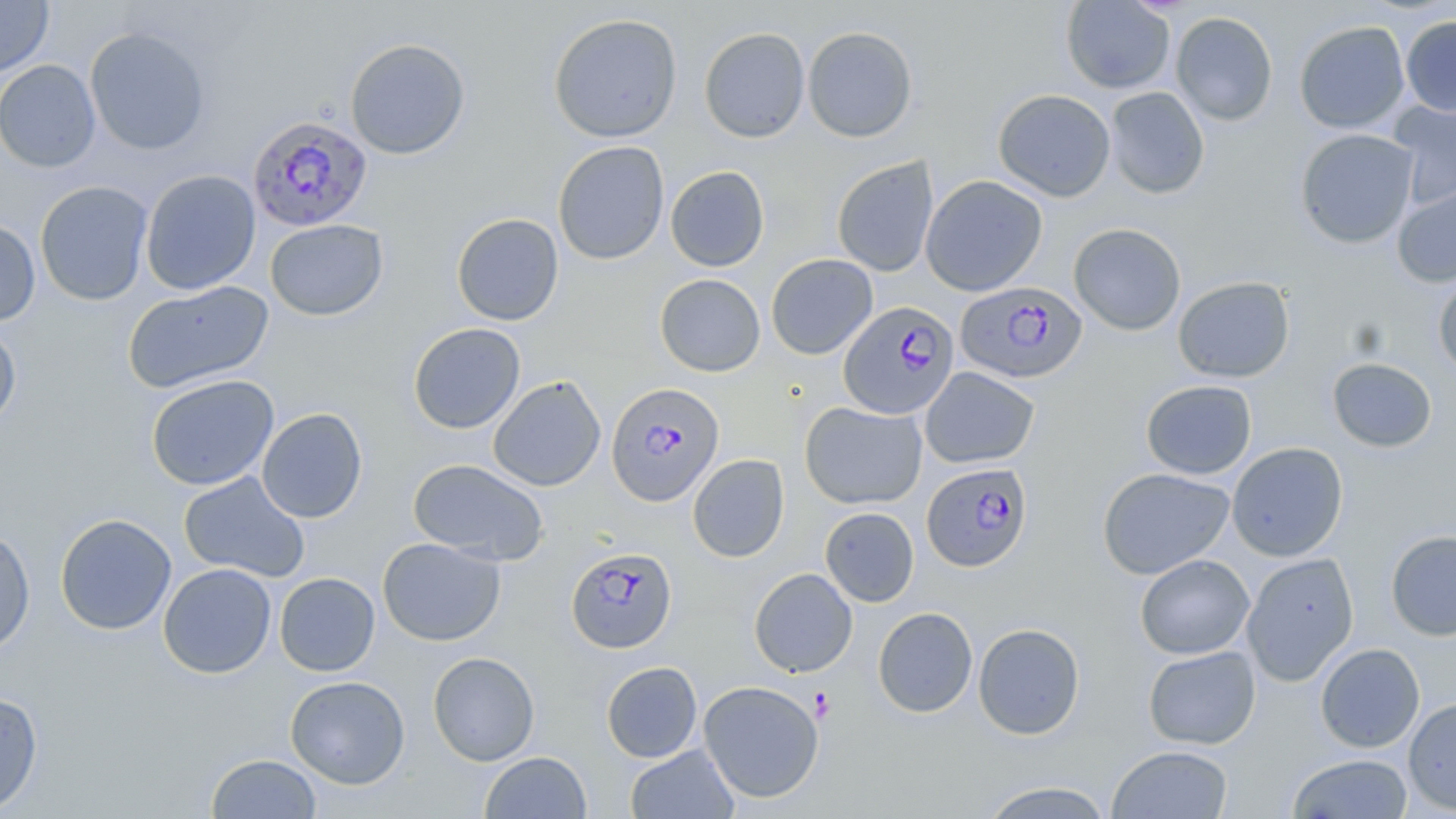
slide_level_diagnosis: Plasmodium falciparum
field_of_view: one of a larger specimen
magnification: 1000x
uninfected_red_blood_cell_locations: 'approximate bounding boxes as (x1,y1)-(x2,y2) corner pairs in pixels: (0,0)-(54,77), (1061,0)-(1176,94), (1170,11)-(1278,126), (548,12)-(683,143), (1400,15)-(1456,117), (1294,20)-(1410,134), (803,26)-(917,142), (84,27)-(210,155), (699,27)-(810,142), (345,37)-(471,160), (0,59)-(101,173), (1104,86)-(1210,199), (993,88)-(1116,202), (1387,100)-(1456,210), (1295,128)-(1420,249), (553,140)-(669,265), (831,156)-(939,278), (665,165)-(769,272), (140,169)-(261,295), (920,175)-(1048,296), (35,180)-(154,306), (1391,180)-(1456,288), (452,212)-(564,325), (265,218)-(388,321), (0,220)-(41,326), (1068,223)-(1187,335), (765,254)-(878,359), (654,273)-(765,377), (1433,273)-(1456,379), (1173,276)-(1295,382), (122,279)-(273,393), (408,322)-(526,434), (0,323)-(21,431), (1326,357)-(1438,452), (920,366)-(1040,469), (146,374)-(279,491), (488,376)-(606,491), (1141,379)-(1257,479), (799,401)-(927,509), (257,407)-(368,523), (1226,442)-(1348,561), (687,454)-(790,562), (408,459)-(549,565), (1097,467)-(1235,580), (178,471)-(310,583), (820,507)-(919,607), (54,513)-(177,635), (0,527)-(35,656), (1385,529)-(1456,641), (377,537)-(506,645), (1241,551)-(1360,687), (1135,554)-(1254,659), (158,563)-(277,678), (749,568)-(857,677), (274,572)-(380,676), (873,607)-(978,718), (973,623)-(1086,740), (1315,643)-(1425,753), (1142,645)-(1261,749), (427,651)-(540,766), (601,661)-(702,762), (285,675)-(410,789), (698,680)-(824,803), (0,692)-(42,815), (1403,697)-(1456,814), (625,744)-(740,818), (1106,745)-(1234,819), (480,751)-(591,818), (206,753)-(322,818), (1287,753)-(1413,818), (977,780)-(1115,819)'
platelet_locations: 'approximate bounding boxes as (x1,y1)-(x2,y2) corner pairs in pixels: (810,687)-(835,720)'
plasmodium_falciparum_infected_red_blood_cell_locations: 'approximate bounding boxes as (x1,y1)-(x2,y2) corner pairs in pixels: (251,115)-(376,233), (955,281)-(1087,384), (838,301)-(959,419), (606,381)-(725,507), (921,463)-(1032,572), (566,546)-(677,653)'
image_size: 1456×819 pixels
preparation: thin blood smear
stain: May-Grünwald-Giemsa
modality: light microscopy